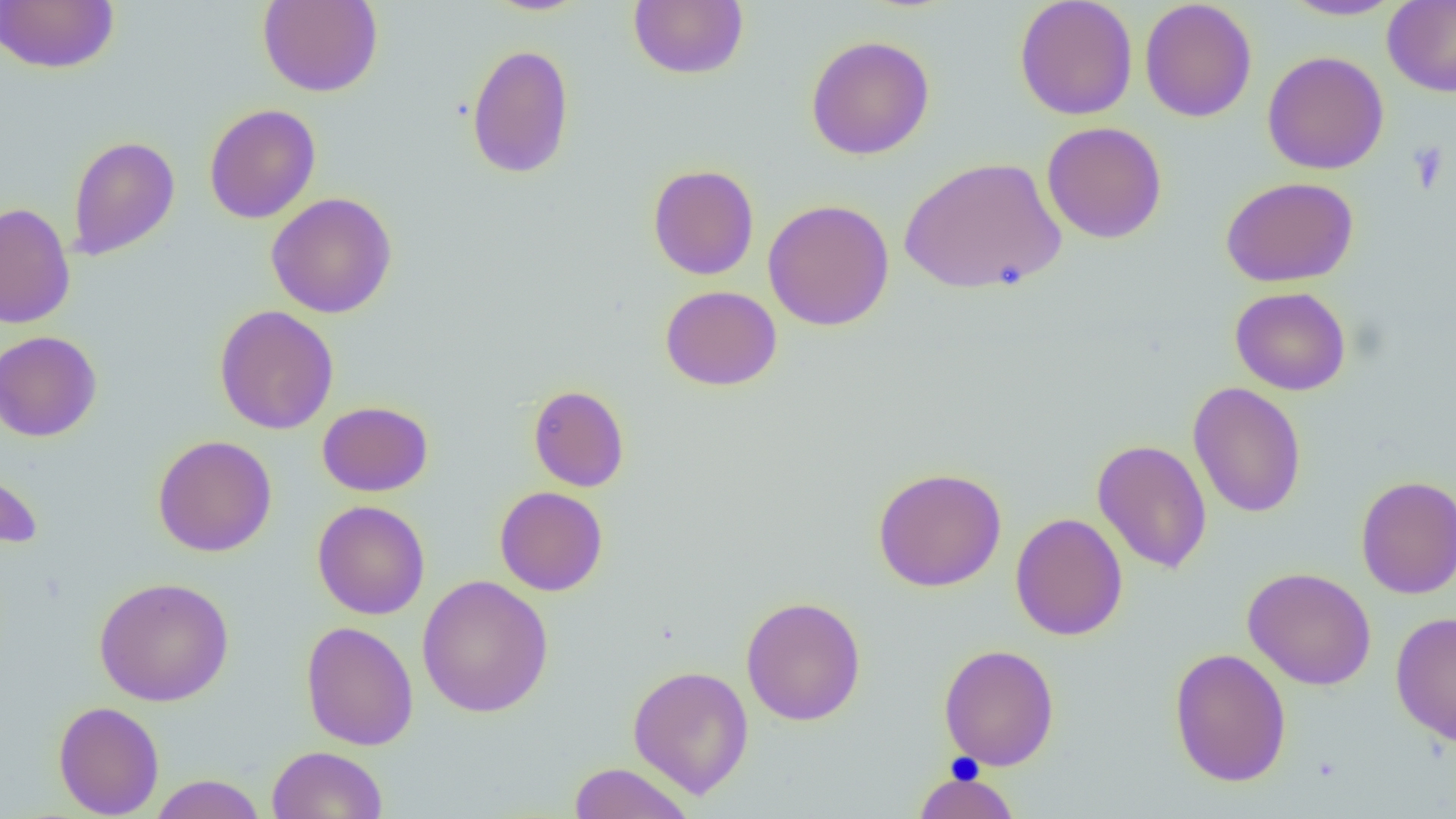

slide-level diagnosis = no evidence of blood parasites
field of view = one of a larger specimen
preparation = thin blood film
magnification = 1000x
modality = light microscopy
uninfected red blood cell locations = approximate bounding boxes as [x1, y1, x2, y2] in pixels: [0, 0, 119, 74], [257, 0, 383, 97], [481, 0, 593, 16], [1014, 0, 1138, 121], [1279, 0, 1402, 20], [628, 1, 749, 80], [1139, 1, 1258, 123], [1382, 1, 1456, 97], [805, 35, 935, 160], [466, 42, 575, 179], [1262, 51, 1389, 175], [204, 103, 321, 224], [1041, 121, 1168, 244], [67, 135, 180, 261], [899, 156, 1068, 295], [647, 163, 759, 280], [1221, 176, 1358, 287], [265, 192, 398, 318], [763, 199, 894, 331], [0, 202, 76, 330], [660, 285, 782, 391], [1230, 286, 1351, 395], [214, 305, 339, 434], [0, 331, 102, 442], [1187, 381, 1307, 519], [528, 385, 629, 492], [317, 401, 433, 497], [152, 435, 277, 557], [1092, 439, 1212, 575], [0, 461, 44, 550], [872, 467, 1007, 592], [1355, 475, 1456, 598], [494, 486, 608, 596], [313, 500, 430, 620], [1009, 512, 1128, 641], [1242, 567, 1377, 690], [416, 575, 553, 718], [93, 576, 234, 706], [740, 596, 867, 726], [1390, 611, 1456, 747], [300, 620, 419, 751], [938, 643, 1059, 770], [1169, 647, 1291, 787], [628, 664, 754, 799], [53, 701, 164, 818], [267, 746, 388, 818], [567, 761, 695, 819], [912, 769, 1021, 819], [149, 774, 266, 818]
platelet locations = approximate bounding boxes as [x1, y1, x2, y2] in pixels: [1406, 140, 1451, 194]
image size = 1456×819 pixels